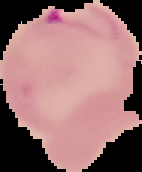
Summary:
  - Malaria status: parasitized
  - Image type: segmented cell region on a black background
  - Preparation: thin blood film
  - Image size: 142×172 pixels